Comment on the morphology of the red blood cells.
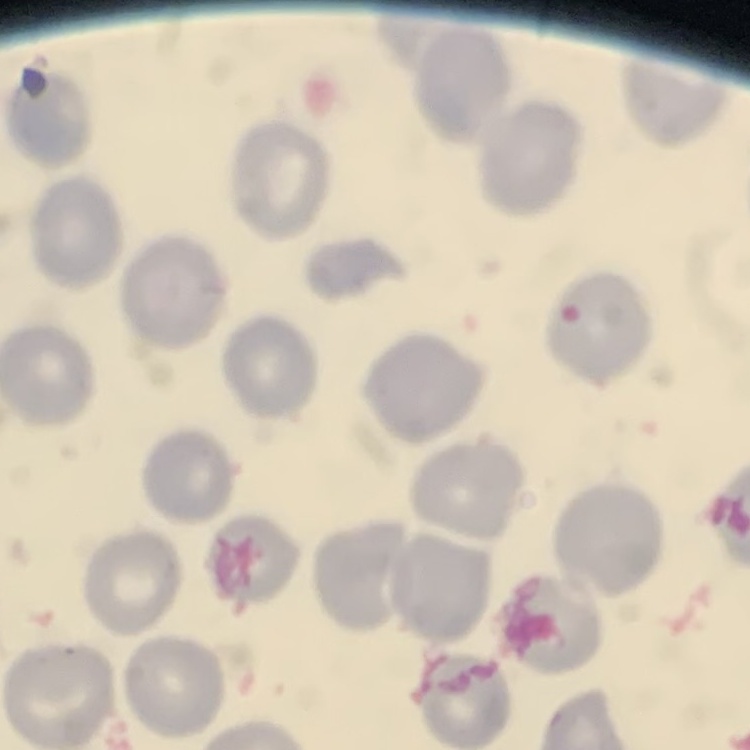
They show no rouleaux formation.

Summary:
  - Preparation: thin peripheral smear
  - Image type: one tile cut from a larger photomicrograph
  - Stain: Field's or Giemsa